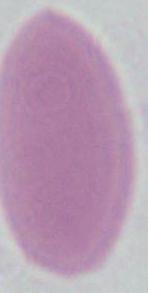
modality: photomicrograph
magnification: 1000x
identification: red blood cell